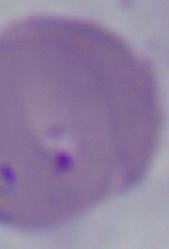

Summary:
  - Magnification: 1000x
  - Identification: Babesia
  - Modality: micrograph